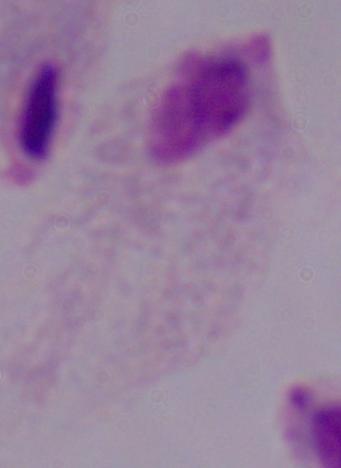
identification = trichomonad
magnification = 1000x
modality = photomicrograph